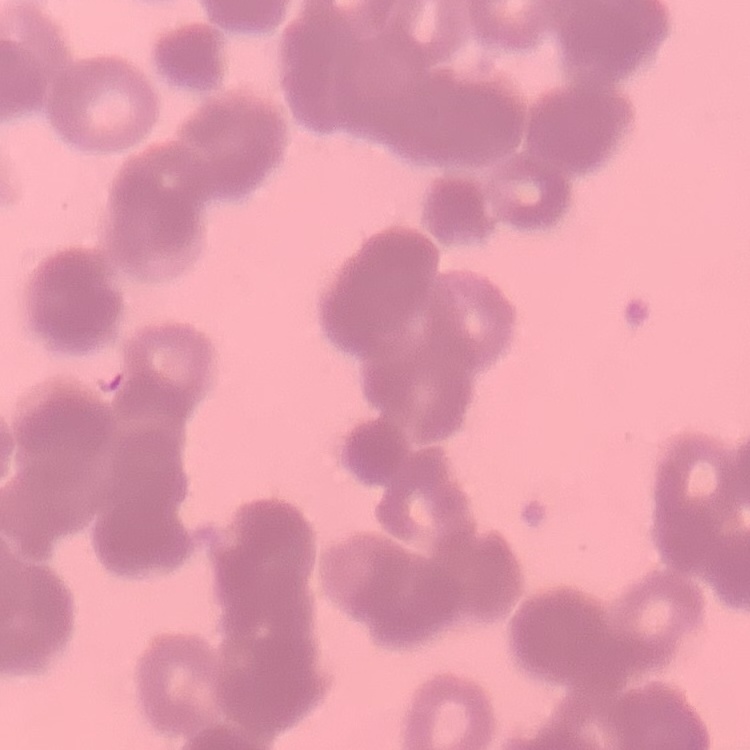
red blood cell morphology = rouleaux formation
preparation = thin blood smear
stain = Field's or Giemsa
image type = square crop of a larger photomicrograph